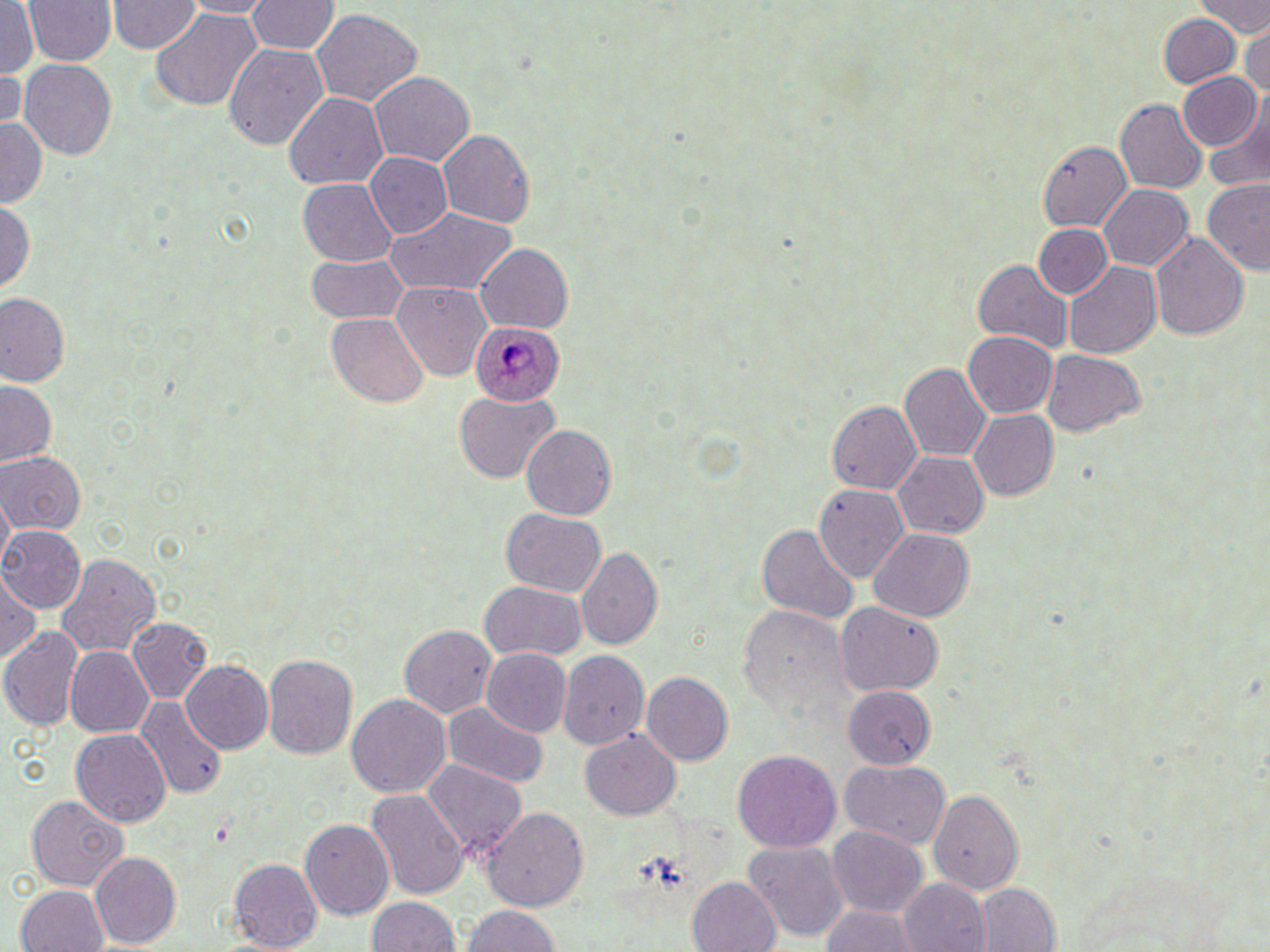
slide-level diagnosis = Plasmodium ovale
field of view = one of a larger specimen
stain = May-Grünwald-Giemsa
image size = 1270×952 pixels
uninfected red blood cell locations = approximate bounding boxes as [x1, y1, x2, y2] in pixels: [21, 0, 118, 66], [179, 0, 277, 17], [245, 0, 340, 58], [1201, 1, 1269, 37], [106, 2, 200, 55], [0, 3, 39, 80], [311, 7, 422, 105], [151, 8, 262, 111], [1157, 14, 1242, 87], [1241, 22, 1269, 97], [223, 43, 328, 150], [18, 57, 118, 160], [0, 69, 26, 137], [369, 70, 475, 166], [1176, 71, 1263, 150], [284, 91, 388, 189], [1205, 96, 1270, 193], [1116, 99, 1208, 193], [0, 120, 46, 208], [436, 129, 535, 229], [1038, 141, 1137, 231], [365, 152, 453, 238], [297, 177, 397, 266], [1202, 180, 1269, 273], [1100, 184, 1194, 270], [0, 197, 35, 292], [381, 206, 516, 297], [1035, 223, 1110, 297], [1149, 233, 1248, 342], [476, 245, 572, 331], [305, 252, 410, 325], [974, 258, 1073, 353], [1063, 261, 1162, 358], [392, 280, 491, 379], [1, 293, 70, 386], [327, 312, 429, 406], [964, 331, 1057, 417], [1041, 350, 1145, 434], [899, 362, 991, 462], [1, 380, 54, 465], [453, 390, 558, 483], [827, 400, 921, 494], [967, 409, 1060, 501], [520, 424, 617, 519], [0, 451, 85, 535], [894, 452, 988, 538], [814, 483, 910, 581], [0, 490, 14, 569], [500, 507, 606, 596], [756, 523, 860, 624], [0, 525, 86, 610], [867, 527, 975, 622], [577, 546, 663, 650], [57, 552, 162, 656], [0, 569, 40, 665], [478, 582, 589, 663], [835, 601, 943, 695], [739, 603, 845, 715], [128, 617, 212, 703], [398, 624, 498, 718], [0, 626, 83, 730], [64, 646, 154, 737], [480, 647, 571, 735], [556, 649, 649, 748], [262, 654, 357, 759], [183, 660, 274, 753], [640, 672, 735, 765], [840, 683, 937, 769], [346, 693, 452, 797], [127, 695, 226, 805], [442, 702, 548, 788], [71, 727, 171, 829], [581, 728, 680, 819], [731, 748, 842, 853], [838, 758, 951, 849], [423, 759, 527, 858], [927, 787, 1023, 896], [366, 790, 469, 899], [26, 795, 128, 891], [481, 806, 588, 911], [300, 818, 395, 919], [826, 826, 928, 916], [742, 841, 848, 941], [89, 850, 180, 949], [230, 857, 324, 951], [688, 876, 782, 952], [899, 880, 989, 950], [15, 884, 108, 952], [976, 884, 1060, 951], [365, 897, 461, 952], [819, 903, 919, 951], [459, 905, 561, 952]
modality = optical microscopy
magnification = 1000x
Plasmodium ovale-infected red blood cell locations = approximate bounding boxes as [x1, y1, x2, y2] in pixels: [469, 322, 565, 405]
preparation = thin blood smear